Report the malaria status of this cell.
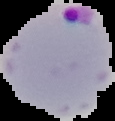

Parasitized.

Image is 115×121 pixels. Segmented cell region on a black background. From a thin blood smear.